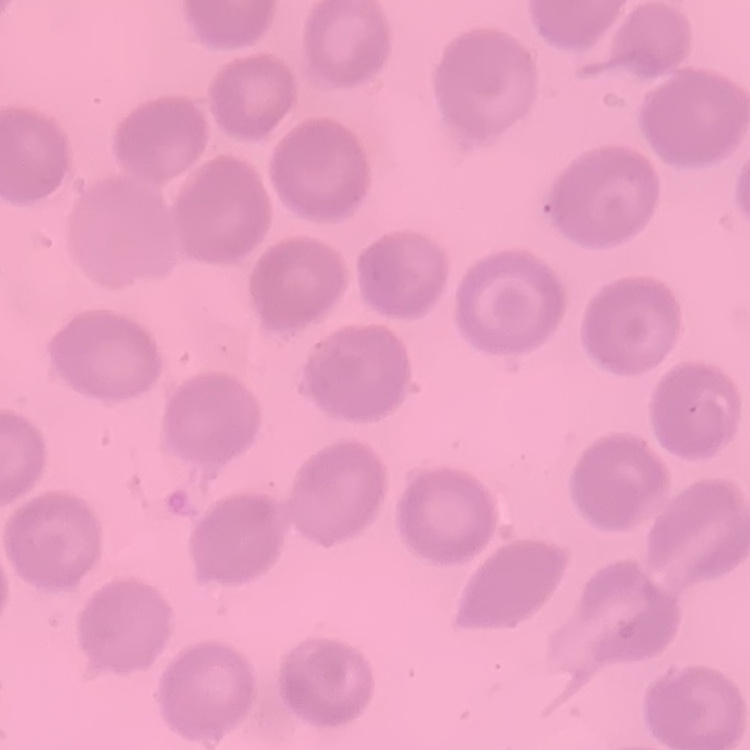
Summary:
  - Red blood cell morphology: no rouleaux formation
  - Stain: Field's or Giemsa
  - Preparation: thin peripheral smear
  - Image type: square crop of a larger photomicrograph